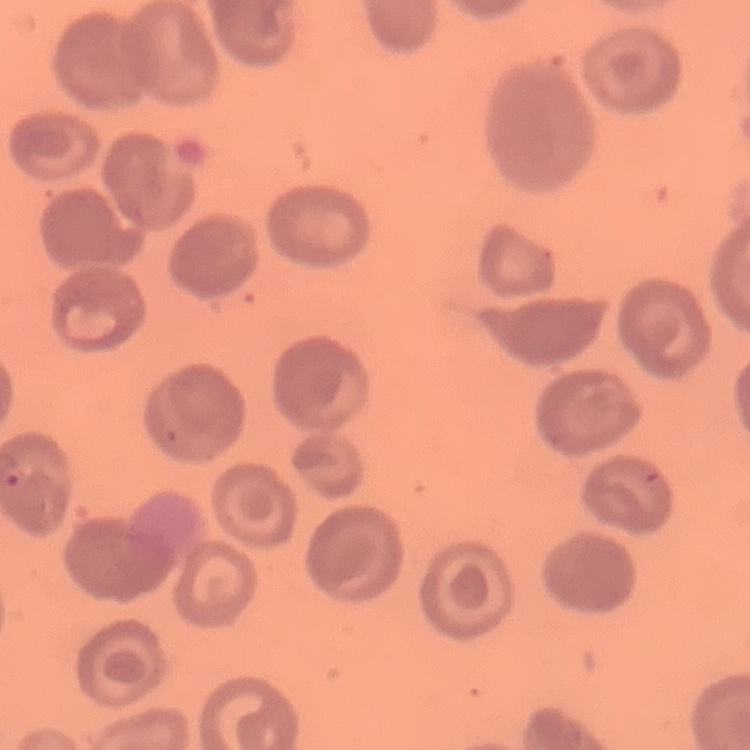

Summary:
  - Erythrocyte morphology: no rouleaux formation
  - Image type: square crop of a larger photomicrograph
  - Stain: Field's or Giemsa
  - Preparation: thin blood smear